Locate every uninfected red blood cell.
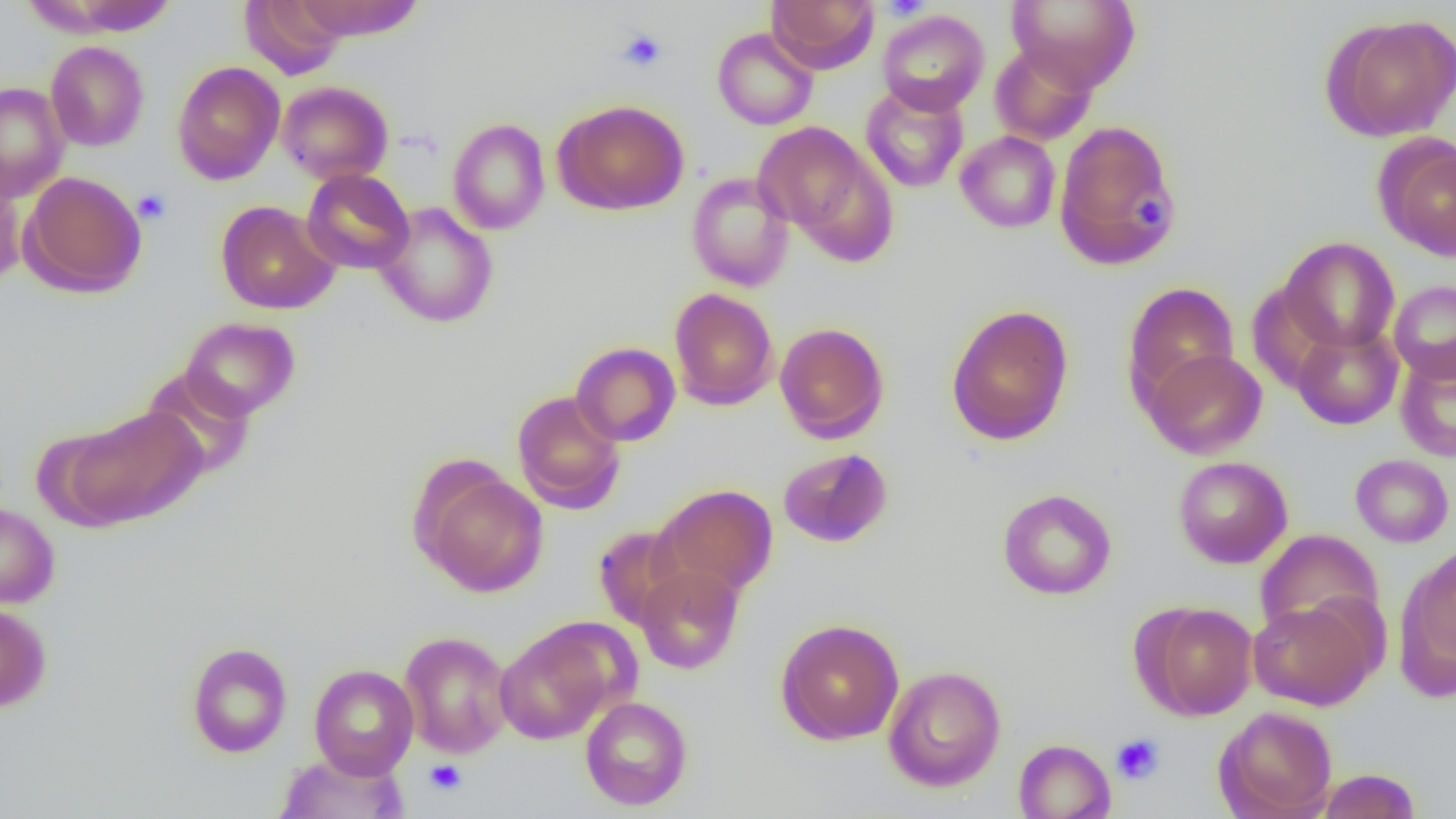

Approximate bounding boxes as named x1/y1/x2/y2 corners in pixels.
Uninfected red blood cells: (x1=36, y1=0, x2=178, y2=36), (x1=239, y1=0, x2=349, y2=79), (x1=290, y1=0, x2=426, y2=41), (x1=767, y1=0, x2=878, y2=73), (x1=1005, y1=0, x2=1141, y2=91), (x1=877, y1=10, x2=989, y2=115), (x1=1323, y1=13, x2=1456, y2=141), (x1=712, y1=28, x2=818, y2=131), (x1=45, y1=40, x2=149, y2=152), (x1=990, y1=43, x2=1097, y2=145), (x1=171, y1=60, x2=286, y2=186), (x1=277, y1=80, x2=393, y2=184), (x1=1, y1=82, x2=69, y2=202), (x1=860, y1=83, x2=969, y2=193), (x1=553, y1=99, x2=689, y2=215), (x1=447, y1=118, x2=550, y2=235), (x1=1053, y1=119, x2=1180, y2=270), (x1=753, y1=121, x2=889, y2=250), (x1=955, y1=131, x2=1061, y2=233), (x1=1376, y1=136, x2=1456, y2=261), (x1=301, y1=168, x2=415, y2=274), (x1=21, y1=170, x2=147, y2=298), (x1=0, y1=172, x2=27, y2=289), (x1=686, y1=172, x2=795, y2=292), (x1=215, y1=200, x2=340, y2=315), (x1=374, y1=202, x2=499, y2=328), (x1=1279, y1=237, x2=1400, y2=353), (x1=1389, y1=280, x2=1456, y2=383), (x1=1123, y1=282, x2=1239, y2=409), (x1=669, y1=288, x2=779, y2=410), (x1=946, y1=304, x2=1074, y2=445), (x1=180, y1=317, x2=300, y2=420), (x1=774, y1=322, x2=889, y2=443), (x1=1291, y1=324, x2=1402, y2=430), (x1=571, y1=342, x2=680, y2=446), (x1=1143, y1=348, x2=1268, y2=459), (x1=1162, y1=350, x2=1276, y2=569), (x1=1395, y1=350, x2=1456, y2=462), (x1=140, y1=366, x2=256, y2=479), (x1=511, y1=390, x2=626, y2=514), (x1=61, y1=407, x2=208, y2=528), (x1=778, y1=448, x2=893, y2=548), (x1=1350, y1=454, x2=1454, y2=547), (x1=1173, y1=456, x2=1293, y2=569), (x1=415, y1=466, x2=549, y2=597), (x1=655, y1=484, x2=778, y2=598), (x1=997, y1=488, x2=1117, y2=600), (x1=0, y1=502, x2=59, y2=609), (x1=592, y1=525, x2=690, y2=630), (x1=1255, y1=529, x2=1384, y2=641), (x1=1401, y1=544, x2=1456, y2=689), (x1=635, y1=565, x2=744, y2=674), (x1=1247, y1=599, x2=1378, y2=710), (x1=0, y1=601, x2=52, y2=712), (x1=1138, y1=601, x2=1258, y2=720), (x1=775, y1=618, x2=905, y2=746), (x1=495, y1=622, x2=618, y2=744), (x1=398, y1=631, x2=514, y2=758), (x1=186, y1=642, x2=292, y2=758), (x1=308, y1=663, x2=419, y2=778), (x1=883, y1=665, x2=1006, y2=792), (x1=579, y1=695, x2=693, y2=810), (x1=1214, y1=706, x2=1338, y2=818), (x1=1013, y1=738, x2=1116, y2=819), (x1=274, y1=749, x2=410, y2=818), (x1=1316, y1=768, x2=1421, y2=819).

Summary:
  - Platelet locations: (x1=881, y1=0, x2=929, y2=20), (x1=617, y1=28, x2=667, y2=72), (x1=133, y1=189, x2=171, y2=224), (x1=1133, y1=193, x2=1170, y2=228), (x1=1110, y1=734, x2=1164, y2=785), (x1=425, y1=759, x2=467, y2=795)
  - Slide-level diagnosis: negative for blood parasites
  - Magnification: 1000x
  - Preparation: thin blood smear
  - Field of view: one of a larger specimen
  - Modality: optical microscopy
  - Image size: 1456×819 pixels